Name the parasite shown.
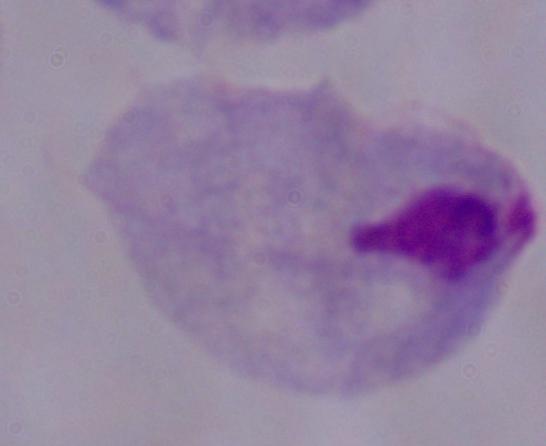
A trichomonad.

magnification = 1000x
modality = photomicrograph